Assess this cell for malaria.
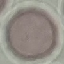
It is uninfected.

Summary:
  - Image type: cell patch, automatically extracted from a larger field of view and resized to 64 × 64 pixels
  - Preparation: thin smear
  - Capture: smartphone camera at the microscope eyepiece
  - Stain: Giemsa